State the blood parasite species.
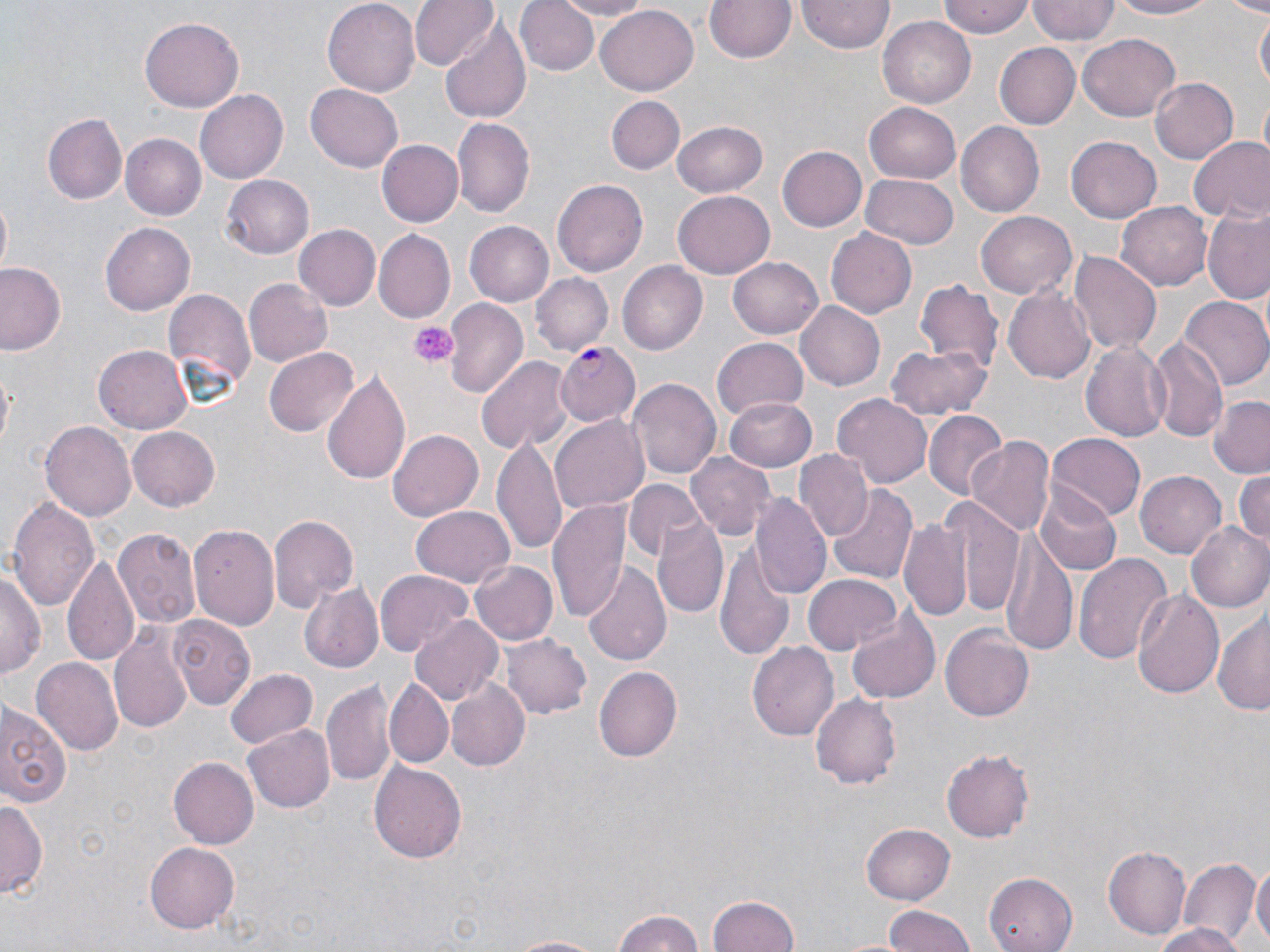
Plasmodium falciparum.

platelet locations = approximate bounding boxes as [x1, y1, x2, y2] in pixels: [409, 322, 459, 367]
magnification = 1000x
modality = optical microscopy
uninfected red blood cell locations = approximate bounding boxes as [x1, y1, x2, y2] in pixels: [323, 0, 419, 92], [410, 0, 497, 72], [517, 0, 597, 76], [547, 0, 656, 18], [706, 0, 794, 64], [798, 0, 895, 53], [937, 0, 1035, 38], [1027, 0, 1118, 44], [1108, 0, 1225, 21], [1224, 0, 1270, 15], [596, 4, 698, 95], [1253, 11, 1269, 89], [140, 16, 244, 112], [879, 16, 975, 108], [439, 17, 531, 124], [1079, 35, 1180, 120], [994, 42, 1080, 131], [1150, 77, 1238, 165], [305, 84, 405, 172], [196, 89, 288, 184], [607, 96, 684, 174], [864, 100, 961, 181], [43, 113, 127, 205], [454, 118, 534, 215], [672, 120, 770, 197], [957, 122, 1045, 216], [120, 133, 208, 219], [1067, 135, 1163, 222], [1187, 138, 1270, 224], [376, 139, 463, 227], [776, 146, 867, 233], [862, 172, 959, 249], [222, 175, 313, 259], [552, 178, 648, 275], [672, 191, 773, 279], [0, 196, 12, 277], [1118, 201, 1212, 292], [1203, 210, 1270, 303], [977, 211, 1076, 298], [466, 221, 558, 306], [101, 222, 195, 315], [295, 225, 381, 311], [827, 228, 916, 320], [376, 230, 457, 323], [1068, 250, 1161, 355], [727, 257, 823, 339], [618, 261, 707, 355], [0, 262, 67, 356], [531, 272, 613, 355], [243, 278, 332, 368], [914, 278, 1004, 374], [1005, 287, 1095, 382], [163, 289, 256, 403], [1179, 297, 1269, 392], [443, 299, 528, 398], [795, 300, 885, 391], [1149, 336, 1229, 444], [711, 337, 808, 421], [1081, 338, 1173, 443], [886, 341, 991, 421], [95, 343, 194, 433], [263, 346, 357, 438], [477, 356, 574, 453], [321, 370, 410, 484], [629, 375, 720, 479], [833, 393, 934, 490], [1209, 394, 1270, 479], [724, 396, 817, 470], [924, 411, 1006, 500], [549, 417, 648, 515], [41, 422, 135, 522], [125, 425, 220, 513], [388, 427, 484, 518], [1047, 434, 1145, 520], [493, 437, 568, 552], [968, 437, 1056, 538], [686, 451, 773, 541], [795, 452, 872, 542], [1136, 471, 1228, 559], [1232, 471, 1269, 551], [626, 480, 703, 562], [828, 486, 918, 583], [1034, 487, 1121, 575], [10, 495, 99, 614], [751, 495, 832, 599], [549, 498, 633, 620], [938, 498, 1023, 618], [411, 506, 516, 588], [267, 513, 357, 615], [900, 515, 973, 621], [652, 518, 730, 620], [1186, 520, 1270, 613], [191, 523, 280, 630], [114, 529, 202, 629], [1001, 531, 1077, 651], [715, 537, 798, 663], [64, 553, 141, 669], [1075, 554, 1172, 664], [470, 560, 557, 646], [0, 562, 42, 683], [584, 562, 670, 668], [375, 569, 472, 657], [802, 574, 901, 656], [298, 580, 382, 675], [1131, 589, 1226, 701], [1213, 606, 1270, 715], [847, 607, 940, 703], [409, 614, 503, 706], [171, 615, 254, 709], [110, 624, 193, 736], [941, 626, 1034, 723], [502, 633, 593, 721], [749, 641, 842, 740], [32, 657, 123, 756], [7, 661, 102, 795], [226, 668, 318, 750], [595, 668, 682, 761], [323, 677, 396, 787], [445, 679, 529, 773], [384, 680, 452, 769], [811, 691, 905, 788], [0, 697, 72, 810], [244, 724, 334, 812], [940, 748, 1036, 843], [169, 756, 258, 850], [369, 759, 467, 867], [0, 797, 44, 899], [862, 824, 956, 903], [143, 840, 240, 934], [1102, 845, 1191, 939], [1181, 858, 1256, 944], [1251, 859, 1270, 949], [981, 872, 1078, 952], [708, 893, 800, 952], [881, 905, 979, 951], [613, 909, 706, 952], [1150, 924, 1246, 952], [500, 934, 608, 952]
field of view = single
preparation = thin blood smear
image size = 1270×952 pixels
stain = May-Grünwald-Giemsa
Plasmodium falciparum-infected red blood cell locations = approximate bounding boxes as [x1, y1, x2, y2] in pixels: [553, 343, 639, 426]